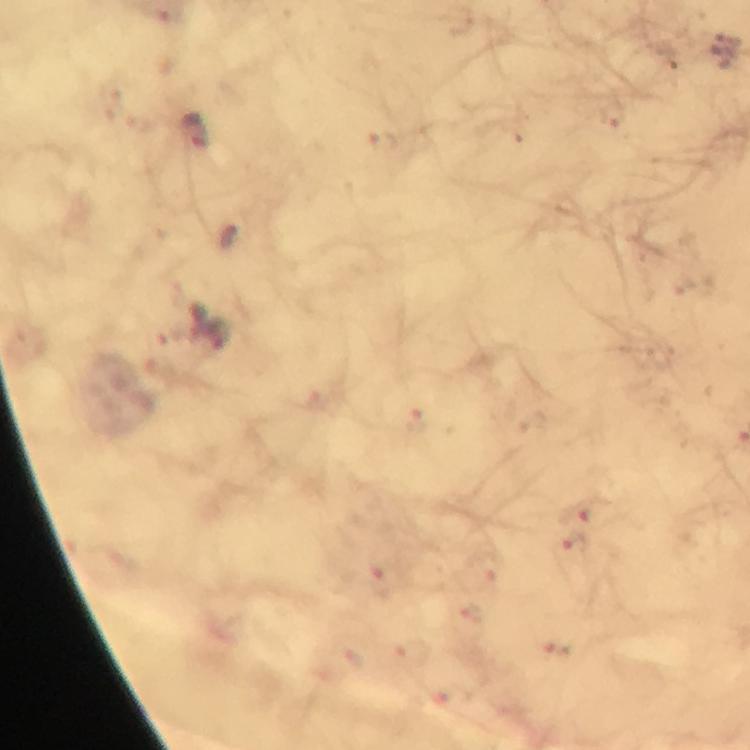

cropped from = a single field of view
stain = Giemsa
capture = smartphone camera through the microscope
malaria parasite locations = approximate centers as (x, y) in pixels: (194, 131), (419, 419), (585, 509), (576, 546), (491, 568), (381, 582), (474, 617), (561, 651)
context = from a diagnostic examination for malaria
immersion oil = applied
image size = 750×750 pixels
preparation = thick blood smear
magnification = 100x